Draw a bounding box around every leukocyte (white blood cell).
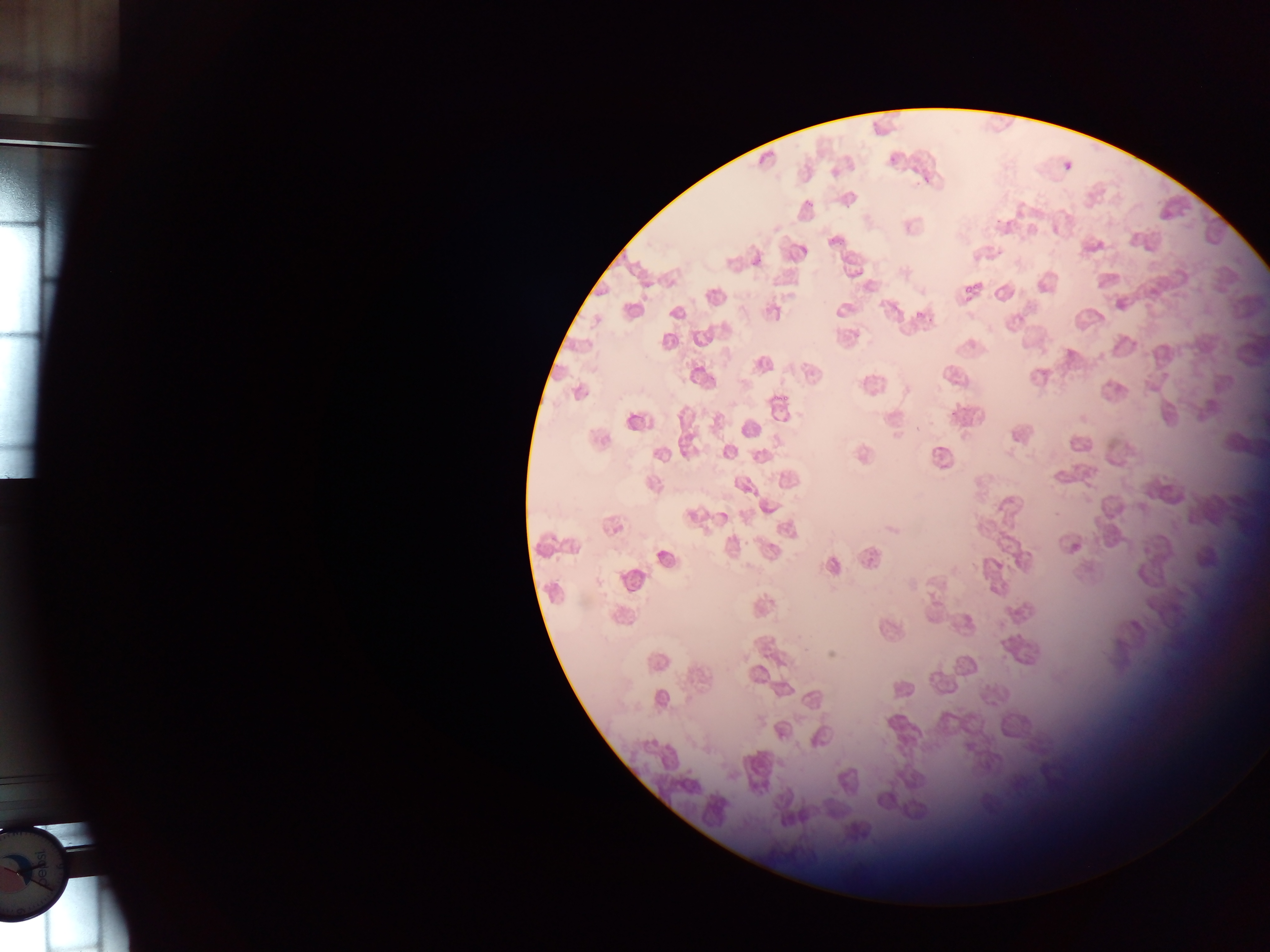
No leukocytes observed.

Approximate bounding boxes as (left, top, right, bottom) in pixels. Malaria parasite locations: (889, 155, 899, 164), (1064, 160, 1074, 172), (1071, 536, 1088, 552). Collected in Ghana. One field of view. Thin blood smear. Image is 1270×952 pixels. Photographed through a microscope with a mobile-phone camera.